Classify this cell by malaria status.
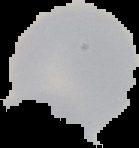
Uninfected.

Summary:
  - Image size: 139×148 pixels
  - Image type: segmented cell region on a black background
  - Preparation: thin blood film